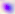

identification = Toxoplasma gondii
magnification = 400x
modality = photomicrograph